Name the parasite shown.
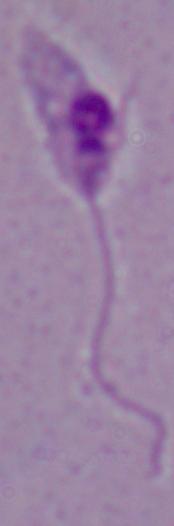

This is Leishmania.

Summary:
  - Magnification: 1000x
  - Modality: micrograph